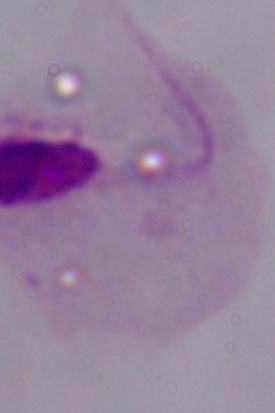 Captured at 1000x magnification. Photomicrograph. A trichomonad is shown.